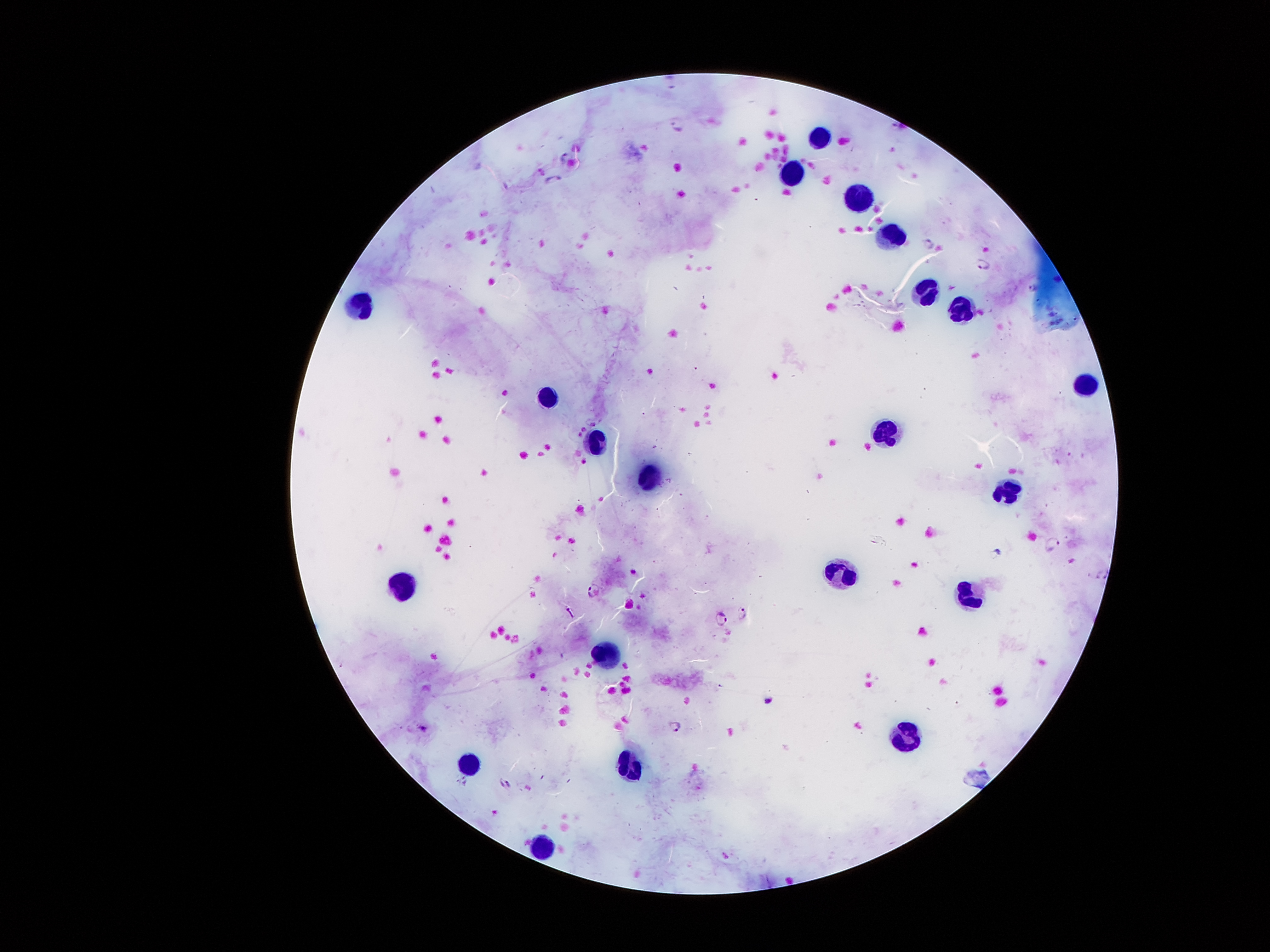
coordinate format = approximate centers as [x, y] in pixels
malaria parasite locations = [563, 154], [552, 178], [926, 243], [983, 265], [1034, 288], [1053, 545], [1102, 575], [593, 590], [743, 614], [721, 619], [676, 727], [422, 728], [504, 786]
leukocyte locations = [818, 135], [796, 173], [854, 199], [888, 236], [930, 295], [357, 303], [962, 311], [1083, 388], [549, 399], [885, 431], [601, 444], [653, 478], [1006, 491], [839, 573], [401, 587], [970, 594], [608, 649], [903, 740], [472, 761], [630, 766], [536, 846]
preparation = thick blood film
stain = Giemsa
capture = smartphone through the microscope eyepiece
field of view = one from this slide
patient malaria status = infected with Plasmodium falciparum
magnification = 100x
image size = 1270×952 pixels